Assess this cell for malaria.
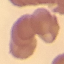

Uninfected.

Giemsa-stained preparation. Thin blood smear. Acquired by smartphone through the microscope eyepiece. Automatically extracted cell patch, resized to 64 × 64 pixels.